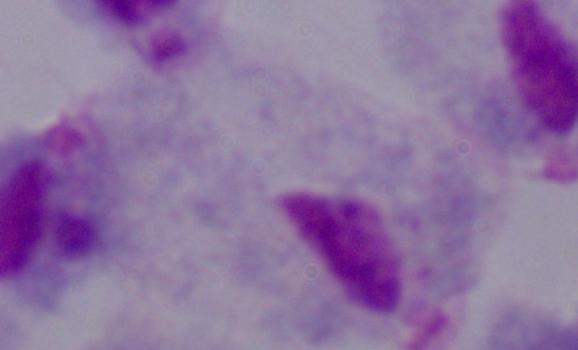

Summary:
  - Identification: trichomonad
  - Modality: micrograph
  - Magnification: 1000x